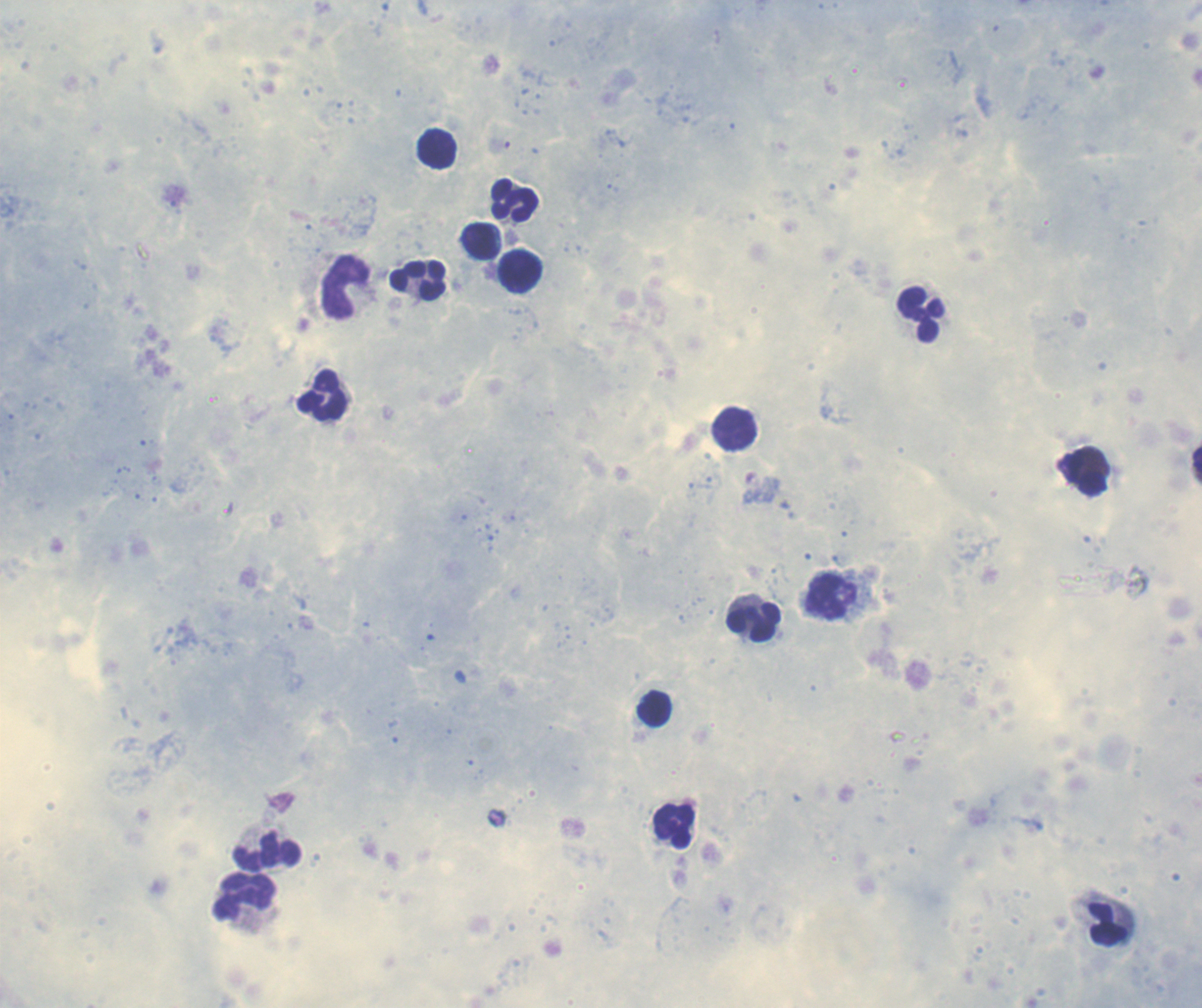

Approximate centers as [x, y] in pixels.
Summary:
  - Leukocyte locations: [437, 149], [515, 201], [479, 242], [520, 272], [418, 281], [346, 288], [922, 314], [323, 396], [735, 429], [1083, 474], [753, 621], [654, 709], [673, 826], [267, 852], [244, 898], [1108, 923]
  - Field of view: single
  - Image size: 1202×1008 pixels
  - Background quality: satisfactory
  - Coloration quality: good
  - Result: negative for malaria parasites
  - Context: previously used in a real diagnosis
  - Stain: Romanowsky
  - Magnification: 100x
  - Preparation: thick blood smear